Assess the morphology of the erythrocytes.
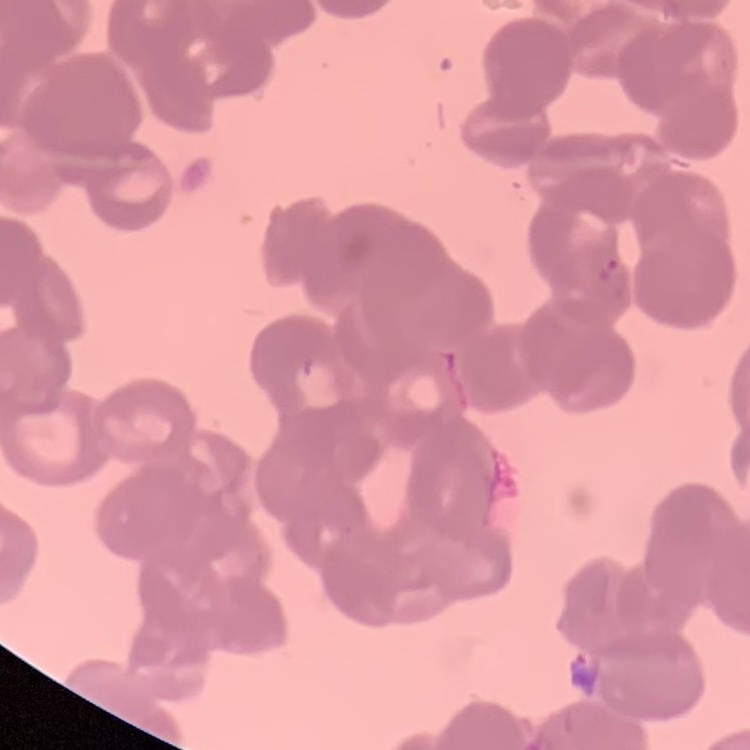

They show rouleaux formation.

{
  "preparation": "thin blood film",
  "stain": "Field's or Giemsa",
  "image_type": "square crop of a larger photomicrograph"
}